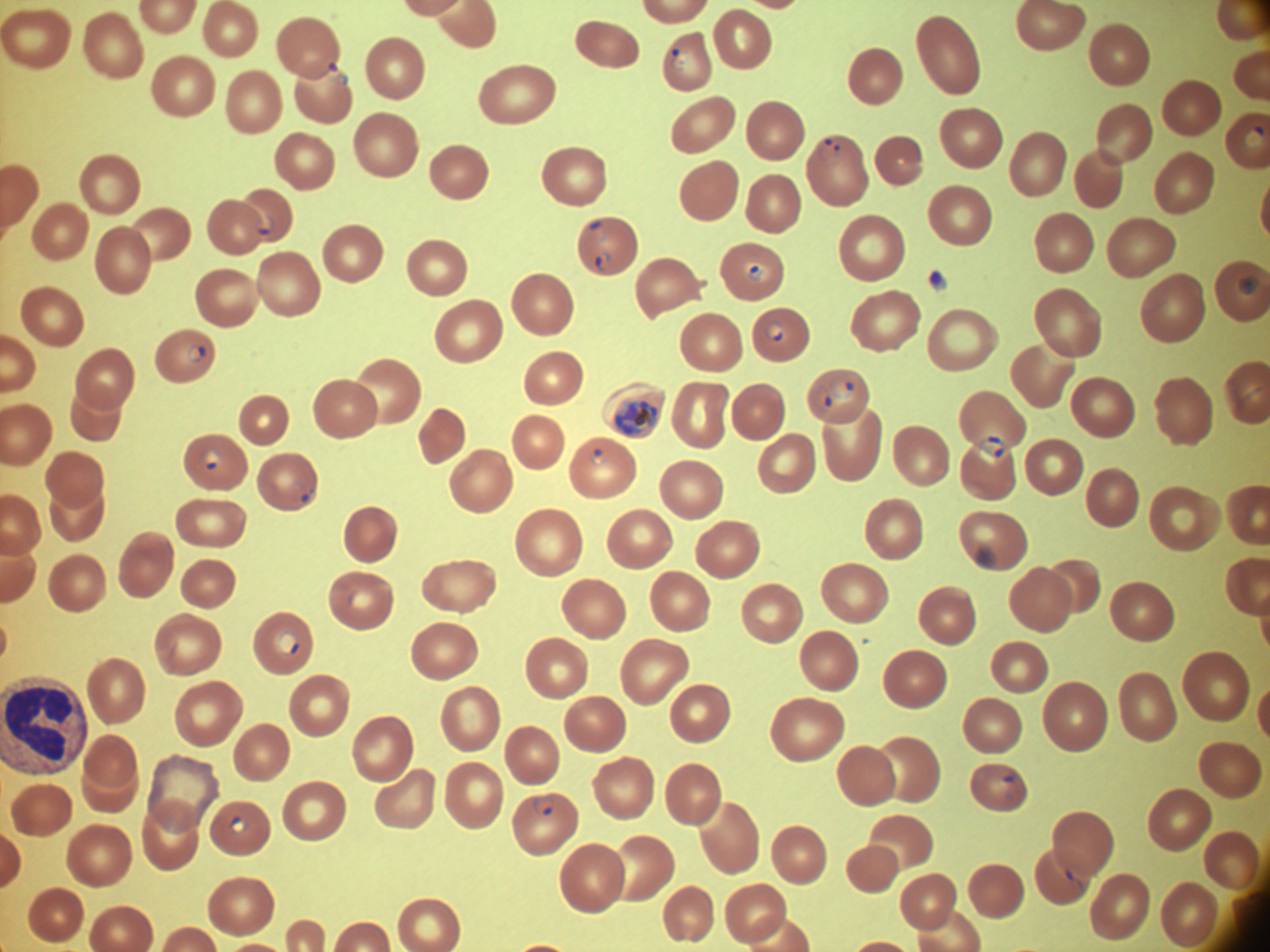
life-cycle stages among the annotated parasites = ring form, trophozoite
magnification = 100x
field of view = one from this slide
ring form locations = approximate bounding boxes as (x1,y1)-(x2,y2) corner pairs in pixels, from the source annotation, which is not necessarily exhaustive: (671,48)-(690,71), (1241,126)-(1266,150), (817,138)-(840,163), (254,216)-(276,236), (588,220)-(608,243), (595,251)-(611,272), (746,262)-(765,282), (1238,275)-(1260,295), (765,321)-(785,342), (187,343)-(206,362), (829,375)-(855,400), (816,386)-(831,411), (979,435)-(1004,458), (201,446)-(221,470), (590,449)-(608,465), (276,630)-(299,657), (534,797)-(555,816), (228,815)-(249,835)
preparation = thin blood smear
image size = 1270×952 pixels
microscope = Leica DM2000 with built-in camera
species = Plasmodium falciparum
stain = Giemsa
trophozoite locations = approximate bounding boxes as (x1,y1)-(x2,y2) corner pairs in pixels, from the source annotation, which is not necessarily exhaustive: (613,400)-(658,436)